Comment on the morphology of the red blood cells.
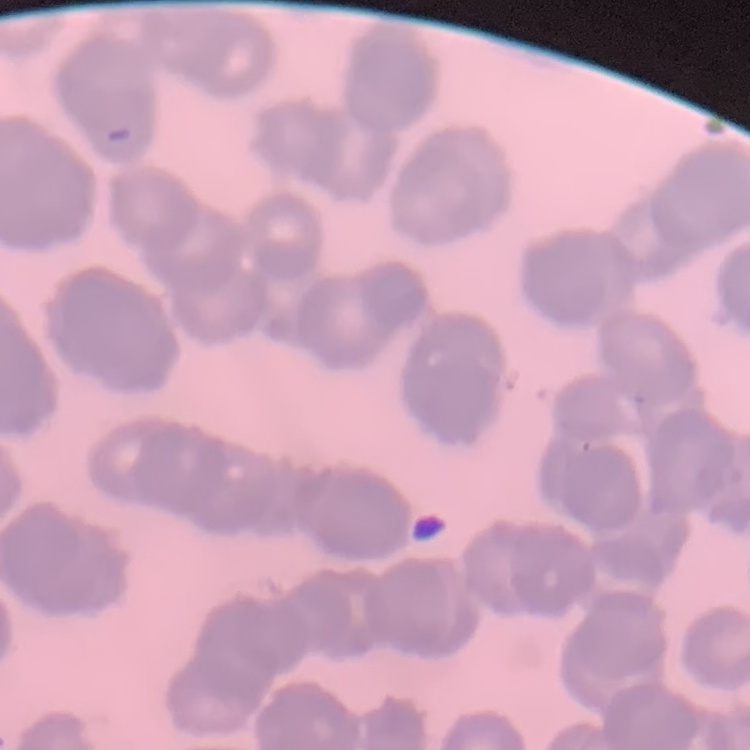
Rouleaux formation.

Summary:
  - Stain: Field's or Giemsa
  - Image type: one tile cut from a larger photomicrograph
  - Preparation: thin peripheral smear